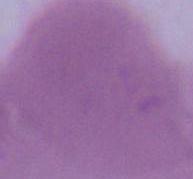

{
  "magnification": "1000x",
  "modality": "photomicrograph",
  "identification": "red blood cell"
}